Locate every Plasmodium falciparum-infected red blood cell.
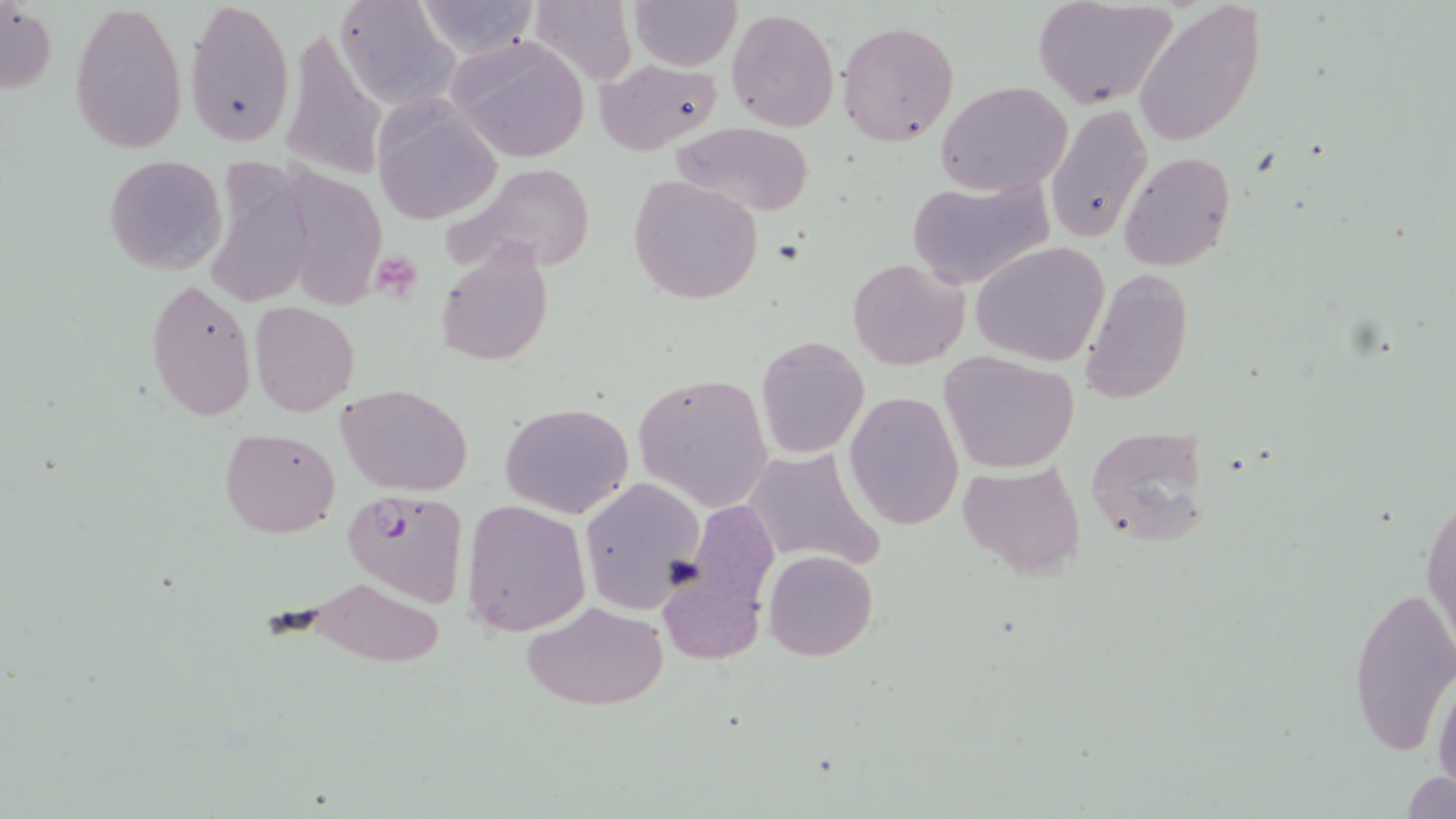
Approximate bounding boxes as (x1,y1)-(x2,y2) corner pairs in pixels.
Plasmodium falciparum-infected red blood cells: (341,488)-(470,606).

slide-level diagnosis = Plasmodium falciparum
stain = May-Grünwald-Giemsa
preparation = thin blood film
field of view = single
modality = light microscopy
magnification = 1000x
image size = 1456×819 pixels
platelet locations = approximate bounding boxes as (x1,y1)-(x2,y2) corner pairs in pixels: (371,255)-(424,301)
uninfected red blood cell locations = approximate bounding boxes as (x1,y1)-(x2,y2) corner pairs in pixels: (70,0)-(187,154), (185,0)-(295,150), (330,0)-(457,109), (410,0)-(543,60), (626,0)-(740,71), (1034,1)-(1181,109), (1134,1)-(1264,147), (0,2)-(57,96), (725,7)-(841,131), (836,19)-(961,148), (444,34)-(591,165), (286,36)-(393,172), (593,58)-(723,154), (938,81)-(1073,195), (370,97)-(499,226), (1045,102)-(1152,244), (669,121)-(816,218), (277,150)-(397,308), (1117,151)-(1235,273), (104,154)-(228,275), (201,161)-(319,310), (443,162)-(596,278), (627,174)-(765,304), (904,175)-(1055,291), (971,241)-(1110,367), (434,244)-(553,366), (847,257)-(968,371), (1080,267)-(1194,404), (146,278)-(256,421), (250,301)-(360,416), (756,335)-(869,459), (938,349)-(1080,474), (633,372)-(774,511), (337,383)-(474,496), (843,391)-(964,530), (499,400)-(635,520), (1084,426)-(1211,547), (220,428)-(340,538), (736,447)-(888,571), (960,460)-(1087,580), (578,476)-(708,612), (1421,477)-(1454,662), (462,498)-(590,636), (764,549)-(878,661), (658,560)-(764,663), (301,577)-(446,667), (1349,581)-(1456,756), (524,601)-(668,710), (1432,667)-(1455,808), (1404,770)-(1453,819)